Give the extent of all Plasmodium ovale-infected red blood cells.
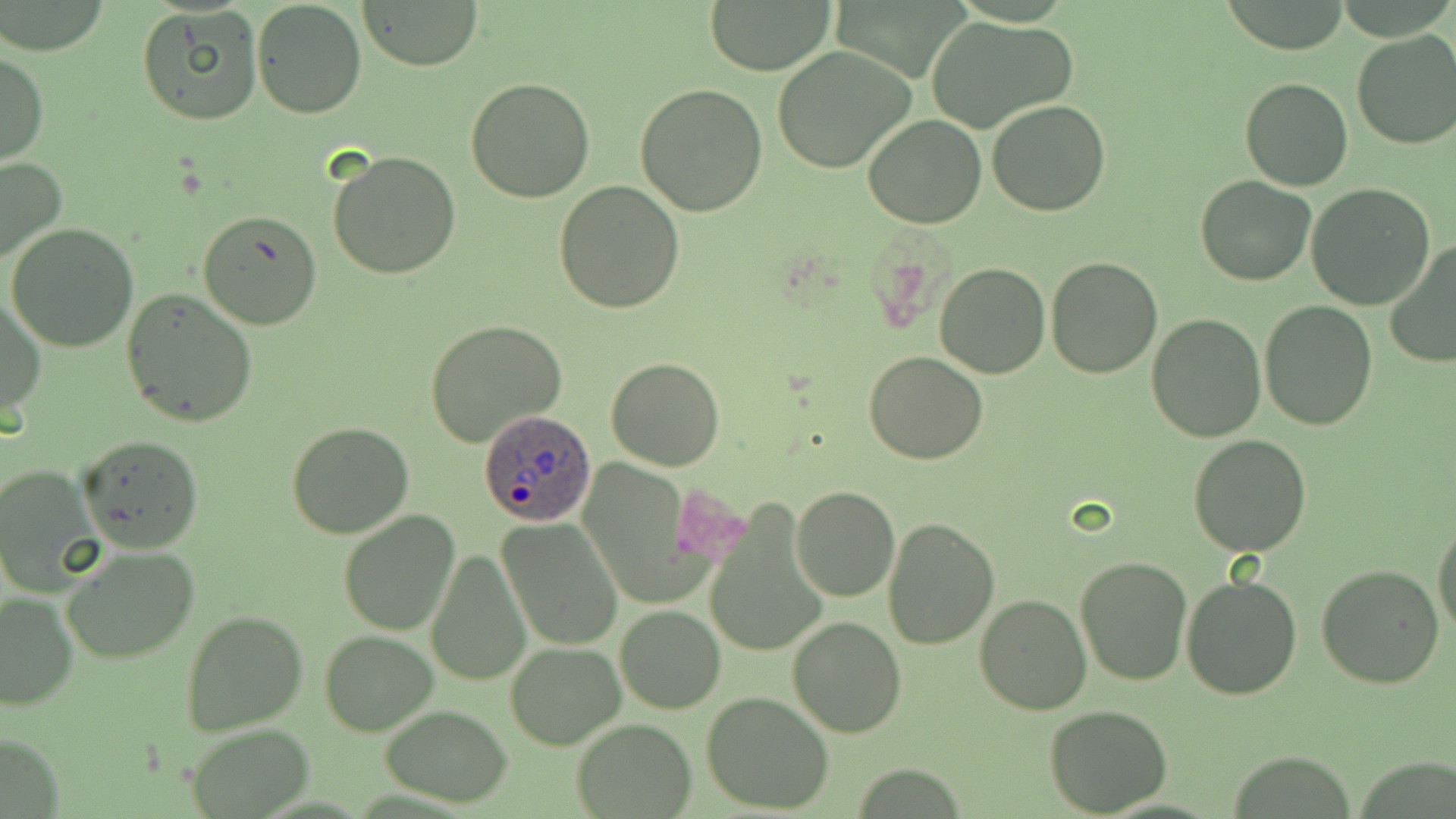
Approximate bounding boxes as (x1,y1)-(x2,y2) corner pairs in pixels.
Plasmodium ovale-infected red blood cells: (479,408)-(597,526).

Summary:
  - Uninfected red blood cell locations: (358,0)-(484,69), (1220,0)-(1352,54), (250,1)-(369,119), (706,2)-(834,75), (137,7)-(263,126), (923,16)-(1076,135), (1351,31)-(1456,150), (772,45)-(920,175), (1,49)-(48,166), (1240,76)-(1353,191), (466,77)-(596,203), (635,81)-(769,217), (987,100)-(1111,218), (864,113)-(987,230), (329,151)-(462,280), (0,156)-(68,268), (1195,175)-(1316,286), (553,180)-(685,313), (1305,183)-(1437,312), (198,210)-(322,331), (6,223)-(139,352), (1383,241)-(1456,370), (1045,254)-(1162,377), (935,263)-(1050,379), (120,289)-(259,430), (2,294)-(45,419), (1259,301)-(1377,429), (1147,312)-(1266,443), (426,319)-(567,448), (863,351)-(988,464), (606,358)-(726,472), (285,421)-(414,538), (76,433)-(204,552), (1188,434)-(1312,556), (0,463)-(103,594), (791,486)-(899,601), (702,501)-(827,662), (338,509)-(461,635), (880,515)-(1000,649), (496,518)-(623,650), (1432,518)-(1456,636), (62,543)-(198,664), (426,546)-(533,687), (1075,554)-(1194,686), (1314,563)-(1445,688), (1181,573)-(1303,700), (0,590)-(79,709), (974,593)-(1091,714), (614,605)-(725,713), (181,610)-(308,737), (787,616)-(907,737), (319,631)-(439,734), (506,642)-(626,749), (701,691)-(836,815), (380,704)-(513,806), (1045,705)-(1172,817), (572,718)-(695,817), (181,723)-(315,816), (2,730)-(61,819)
  - Slide-level diagnosis: Plasmodium ovale
  - Magnification: 1000x
  - Modality: optical microscopy
  - Image size: 1456×819 pixels
  - Preparation: thin blood smear
  - Field of view: single
  - Stain: May-Grünwald-Giemsa